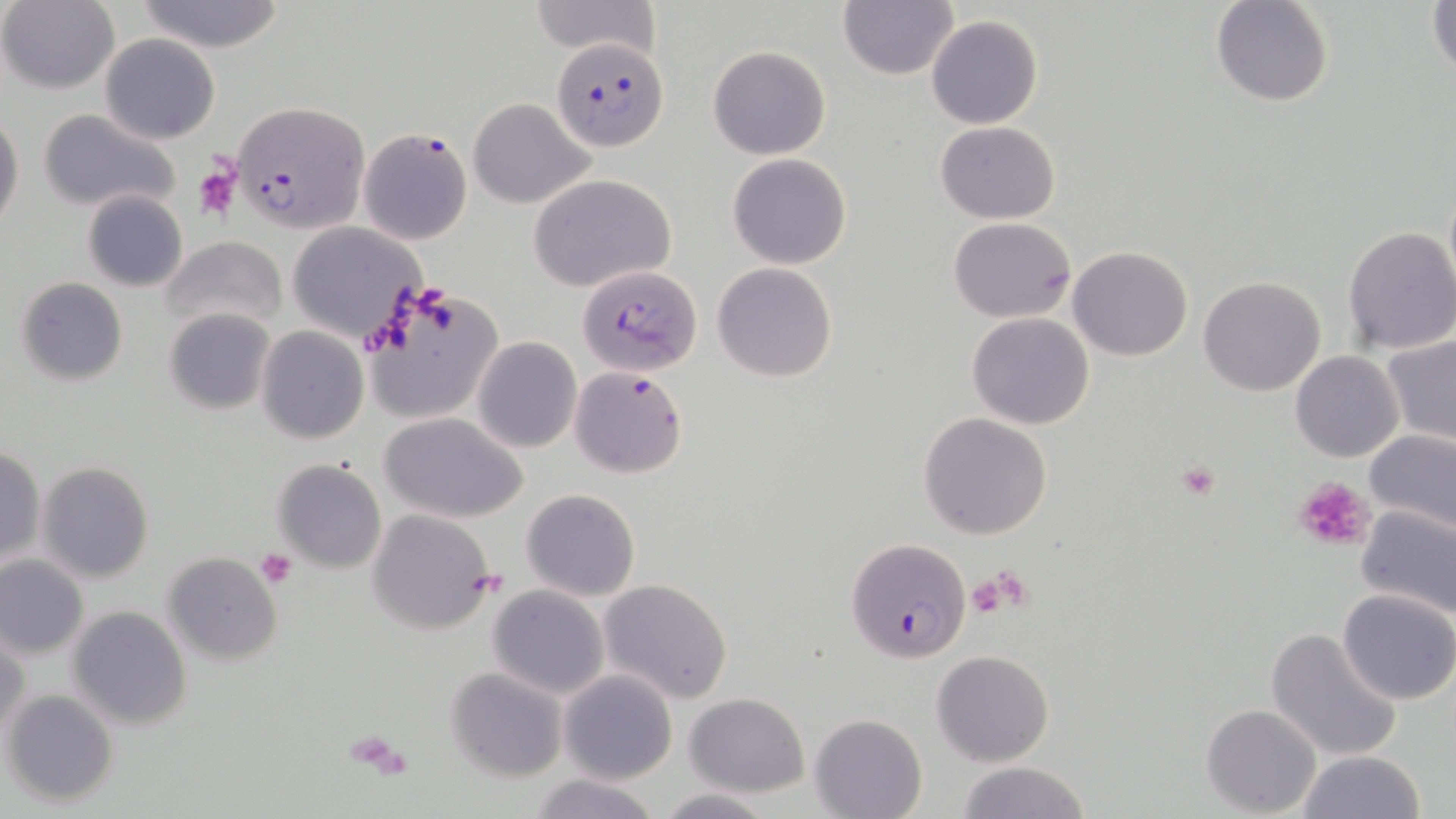
Summary:
  - Coordinate format: approximate bounding boxes as named x1/y1/x2/y2 corners in pixels
  - Platelet locations: (x1=193, y1=165, x2=240, y2=222), (x1=1173, y1=461, x2=1222, y2=504), (x1=1293, y1=474, x2=1377, y2=553), (x1=255, y1=550, x2=296, y2=589), (x1=985, y1=566, x2=1033, y2=612), (x1=968, y1=572, x2=1015, y2=618), (x1=348, y1=733, x2=414, y2=776)
  - Plasmodium falciparum-infected red blood cell locations: (x1=551, y1=35, x2=667, y2=152), (x1=231, y1=101, x2=369, y2=233), (x1=357, y1=125, x2=473, y2=246), (x1=580, y1=265, x2=700, y2=374), (x1=568, y1=365, x2=688, y2=478), (x1=845, y1=537, x2=972, y2=665)
  - Uninfected red blood cell locations: (x1=132, y1=0, x2=290, y2=53), (x1=528, y1=0, x2=659, y2=59), (x1=1211, y1=0, x2=1334, y2=107), (x1=1427, y1=0, x2=1456, y2=81), (x1=0, y1=1, x2=120, y2=93), (x1=837, y1=2, x2=958, y2=80), (x1=926, y1=15, x2=1042, y2=130), (x1=98, y1=33, x2=220, y2=143), (x1=706, y1=45, x2=832, y2=160), (x1=467, y1=98, x2=594, y2=208), (x1=38, y1=108, x2=182, y2=214), (x1=0, y1=113, x2=25, y2=232), (x1=935, y1=121, x2=1061, y2=223), (x1=726, y1=153, x2=852, y2=270), (x1=528, y1=173, x2=676, y2=293), (x1=81, y1=191, x2=188, y2=292), (x1=948, y1=215, x2=1077, y2=322), (x1=285, y1=223, x2=424, y2=343), (x1=1341, y1=225, x2=1456, y2=356), (x1=162, y1=235, x2=288, y2=334), (x1=1067, y1=246, x2=1195, y2=361), (x1=711, y1=262, x2=838, y2=383), (x1=1199, y1=275, x2=1326, y2=397), (x1=15, y1=277, x2=128, y2=387), (x1=362, y1=286, x2=503, y2=425), (x1=164, y1=306, x2=277, y2=417), (x1=966, y1=312, x2=1094, y2=428), (x1=256, y1=327, x2=369, y2=444), (x1=1380, y1=333, x2=1456, y2=449), (x1=472, y1=336, x2=582, y2=454), (x1=1290, y1=351, x2=1404, y2=462), (x1=379, y1=412, x2=529, y2=524), (x1=917, y1=412, x2=1053, y2=539), (x1=1364, y1=432, x2=1456, y2=534), (x1=0, y1=444, x2=47, y2=566), (x1=271, y1=458, x2=387, y2=576), (x1=37, y1=461, x2=154, y2=584), (x1=520, y1=488, x2=641, y2=601), (x1=1355, y1=503, x2=1455, y2=620), (x1=366, y1=507, x2=498, y2=635), (x1=162, y1=552, x2=284, y2=664), (x1=0, y1=554, x2=89, y2=658), (x1=597, y1=578, x2=734, y2=703), (x1=487, y1=585, x2=610, y2=699), (x1=1336, y1=589, x2=1456, y2=707), (x1=67, y1=605, x2=192, y2=731), (x1=1264, y1=628, x2=1403, y2=762), (x1=0, y1=630, x2=29, y2=744), (x1=931, y1=649, x2=1054, y2=766), (x1=444, y1=666, x2=568, y2=783), (x1=559, y1=669, x2=677, y2=785), (x1=2, y1=689, x2=119, y2=807), (x1=683, y1=691, x2=809, y2=796), (x1=1200, y1=703, x2=1323, y2=817), (x1=808, y1=713, x2=927, y2=819), (x1=1296, y1=750, x2=1425, y2=819), (x1=952, y1=760, x2=1094, y2=819), (x1=529, y1=773, x2=661, y2=819), (x1=650, y1=788, x2=782, y2=819)
  - Slide-level diagnosis: Plasmodium falciparum
  - Field of view: one of a larger specimen
  - Stain: May-Grünwald-Giemsa
  - Modality: light microscopy
  - Image size: 1456×819 pixels
  - Preparation: thin blood smear
  - Magnification: 1000x